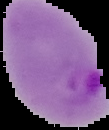
Summary:
  - Malaria status: parasitized
  - Image type: cell region segmented out of the field of view; surrounding area masked to black
  - Image size: 109×130 pixels
  - Preparation: thin blood smear